Assess this cell for malaria.
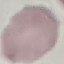
It is uninfected.

Giemsa-stained preparation. Cell patch, automatically extracted from a larger field of view and resized to 64 × 64 pixels. Acquired by smartphone through the microscope eyepiece. Thin blood film.